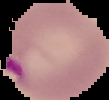
Summary:
  - Malaria status: parasitized
  - Image type: segmented cell region on a black background
  - Preparation: thin blood film
  - Image size: 109×100 pixels